Assess this cell for malaria.
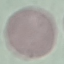
It is uninfected.

Thin blood film. Automatically extracted cell patch, resized to 64 × 64 pixels. Giemsa-stained preparation. Acquired by smartphone through the microscope eyepiece.